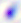 400x magnification. Photomicrograph. Toxoplasma gondii is seen.